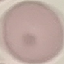
Summary:
  - Malaria status: uninfected
  - Stain: Giemsa
  - Preparation: thin blood film
  - Image type: cell patch, automatically extracted from a larger field of view and resized to 64 × 64 pixels
  - Capture: smartphone through the microscope eyepiece